State the preparation type.
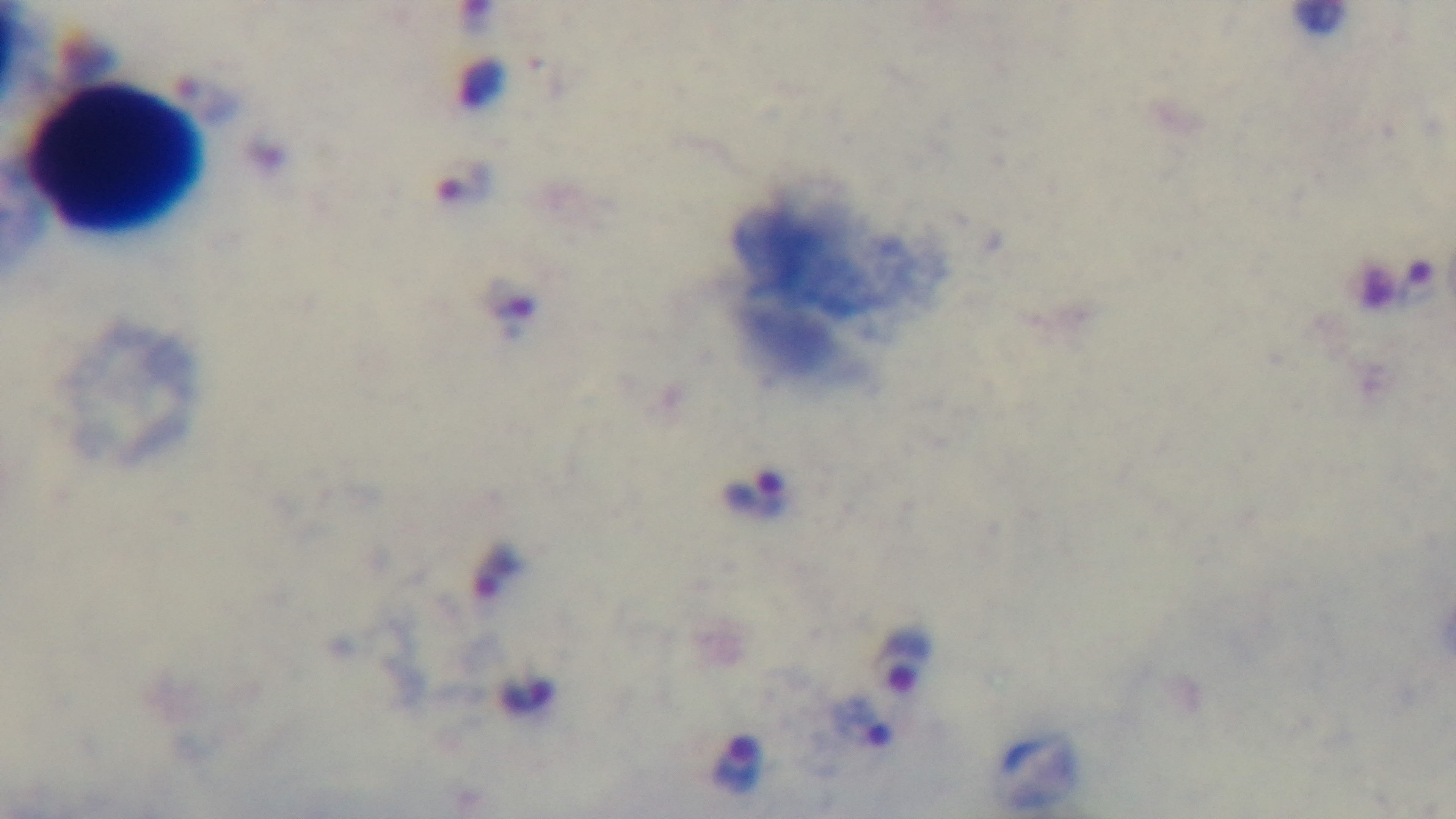

A thick smear.

Summary:
  - Stain: Giemsa
  - Modality: light microscopy
  - Field of view: single
  - Malaria status: positive
  - Objective: 100x oil immersion
  - Capture: mounted 4K digital camera